Evaluate for parasitized red blood cells.
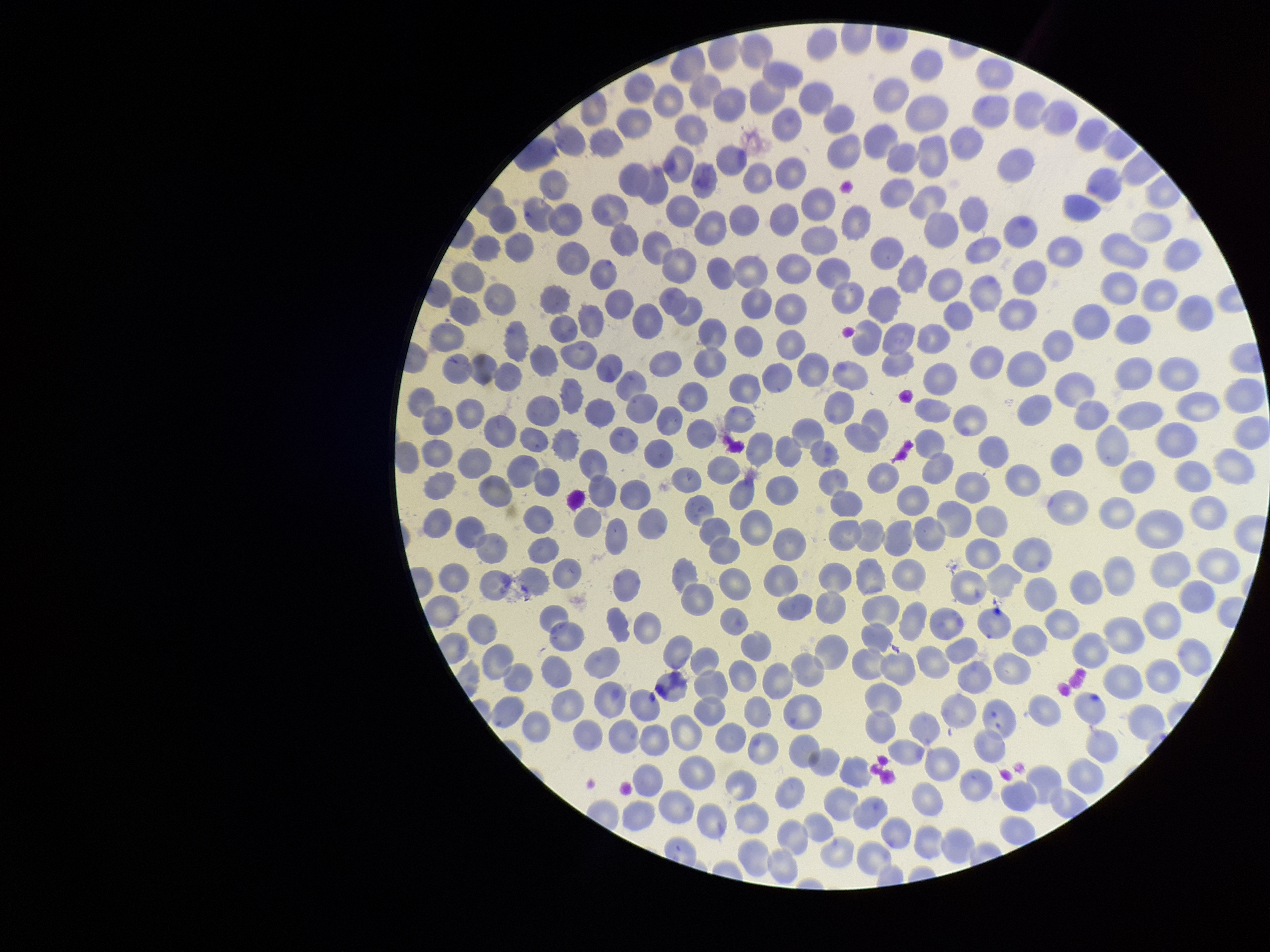

None identified.

field_of_view: one from this slide
patient_malaria_status: negative
preparation: thin smear
red_blood_cell_count: 320
image_size: 1270×952 pixels
capture: smartphone photograph through the microscope eyepiece
parasitized_red_blood_cell_count: 0
stain: Giemsa